State which parasite is depicted.
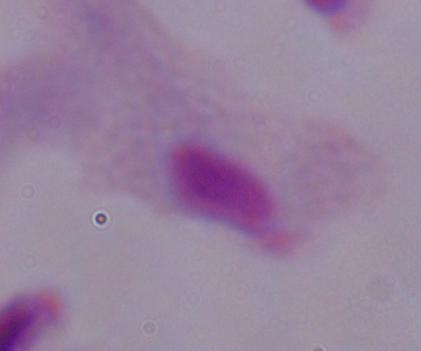
A trichomonad.

Micrograph. 1000x magnification.